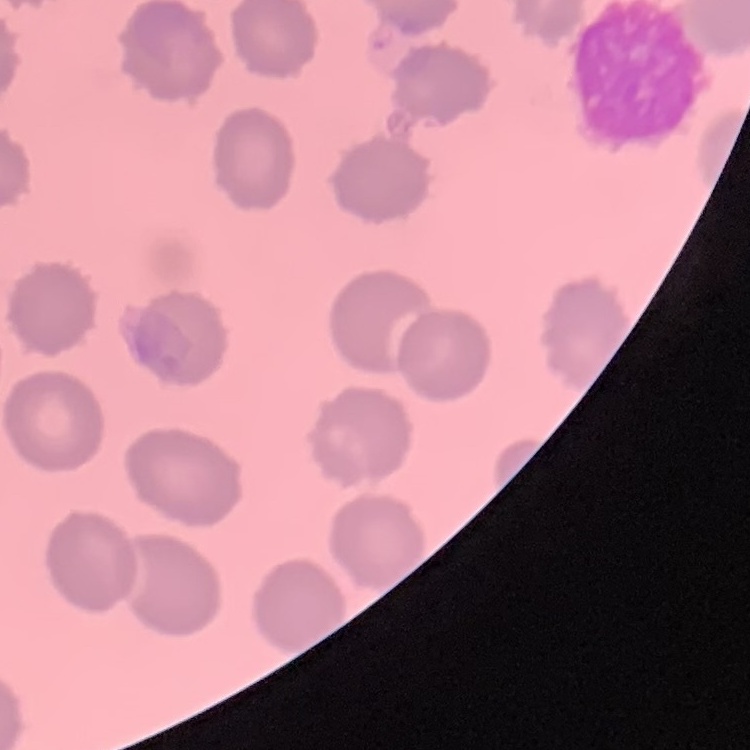
Summary:
  - Erythrocyte morphology: no rouleaux formation
  - Image type: one tile cut from a larger photomicrograph
  - Stain: Field's or Giemsa
  - Preparation: thin blood film